Report the malaria status of this cell.
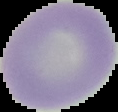
Uninfected.

Image is 118×112 pixels. From a thin blood film. Cell region segmented out of the field of view; the surrounding area is masked to black.